Assess the morphology of the erythrocytes.
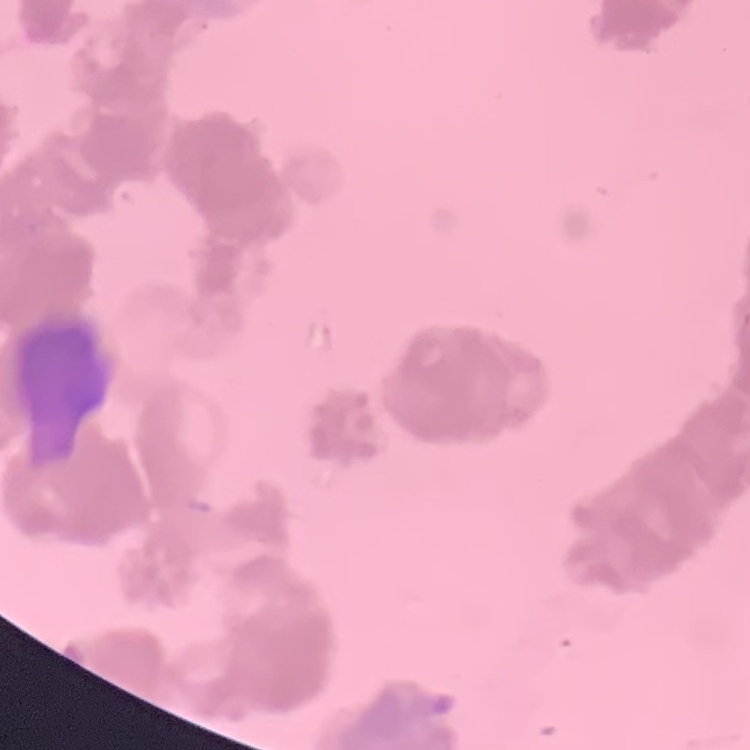

They show rouleaux formation.

Field's or Giemsa stain. Square crop of a larger photomicrograph. Thin blood film.